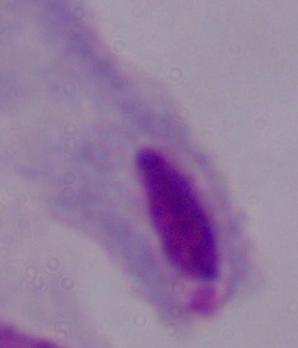
A trichomonad is shown. Photomicrograph. 1000x magnification.